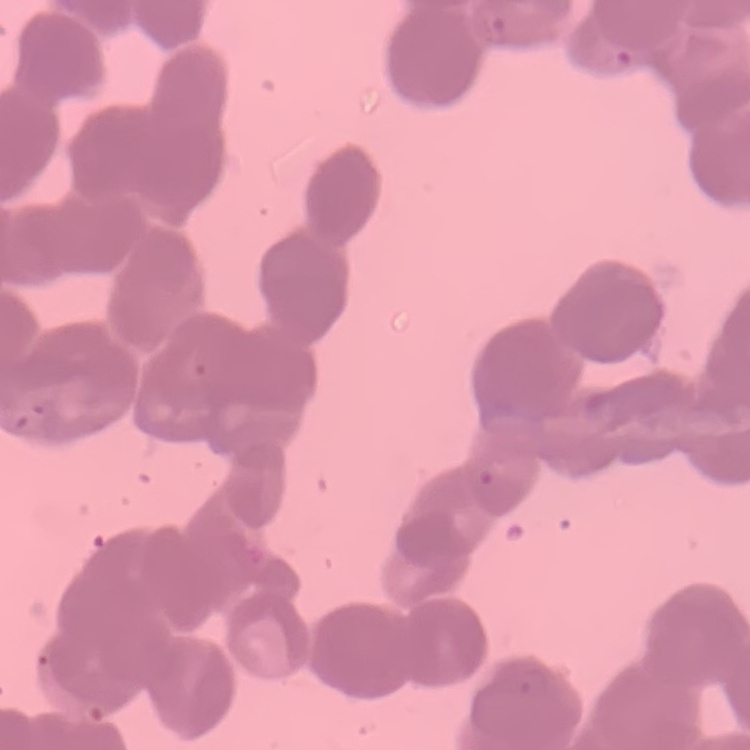

{
  "red_blood_cell_morphology": "rouleaux formation",
  "preparation": "thin peripheral smear",
  "image_type": "one tile cut from a larger photomicrograph",
  "stain": "Field's or Giemsa"
}